State which parasite is depicted.
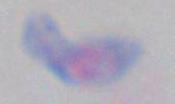

This is Toxoplasma gondii.

Captured at 1000x magnification. Photomicrograph.